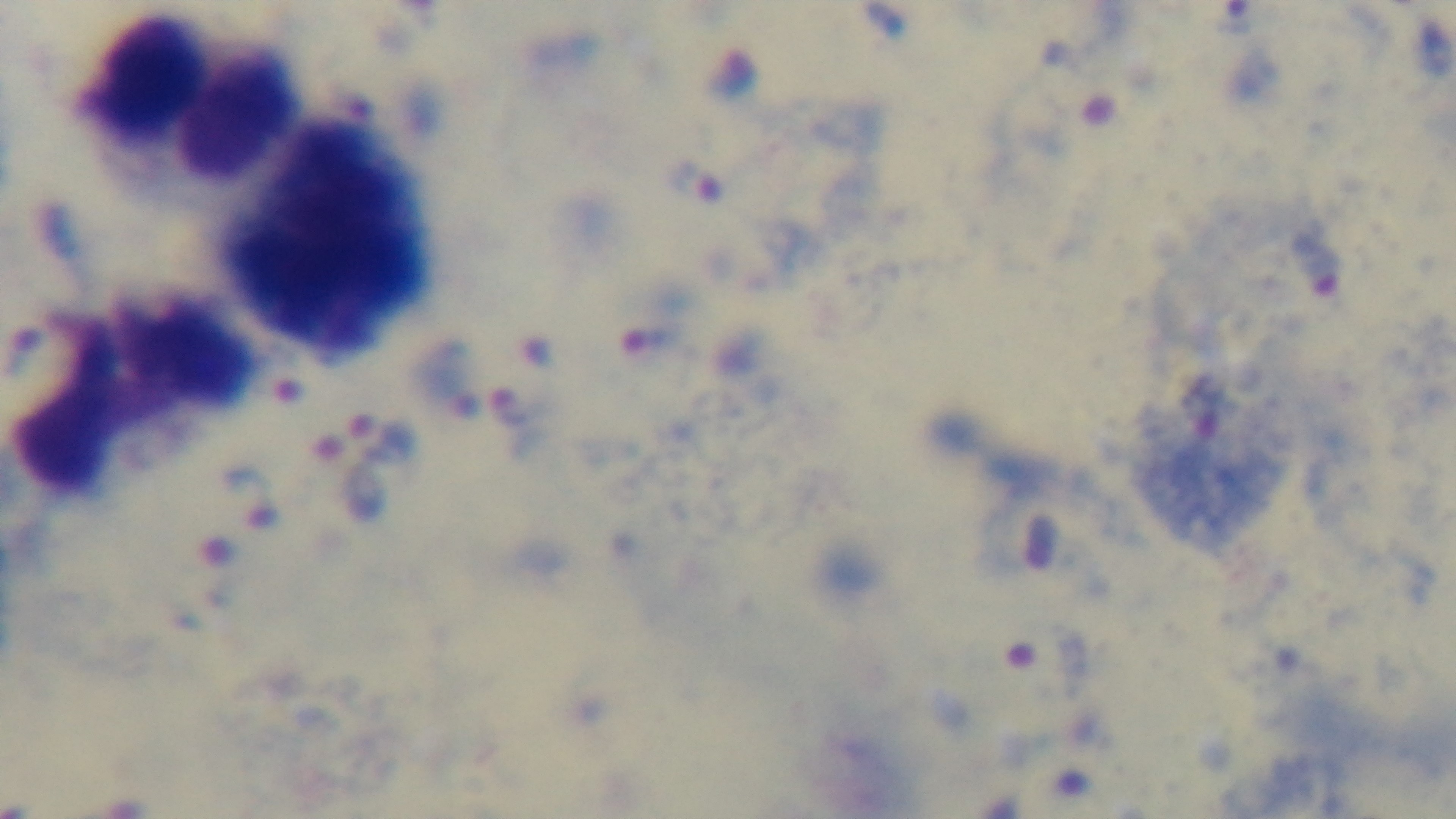
Summary:
  - Preparation: thick smear
  - Modality: light microscopy
  - Field of view: single
  - Stain: Giemsa
  - Objective: 100x oil immersion
  - Malaria status: infected
  - Capture: mounted 4K digital camera